Report the malaria status of this cell.
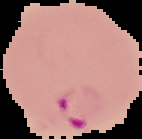

It is parasitized.

Summary:
  - Image size: 142×139 pixels
  - Image type: segmented cell region with the area outside set to black
  - Preparation: thin blood film